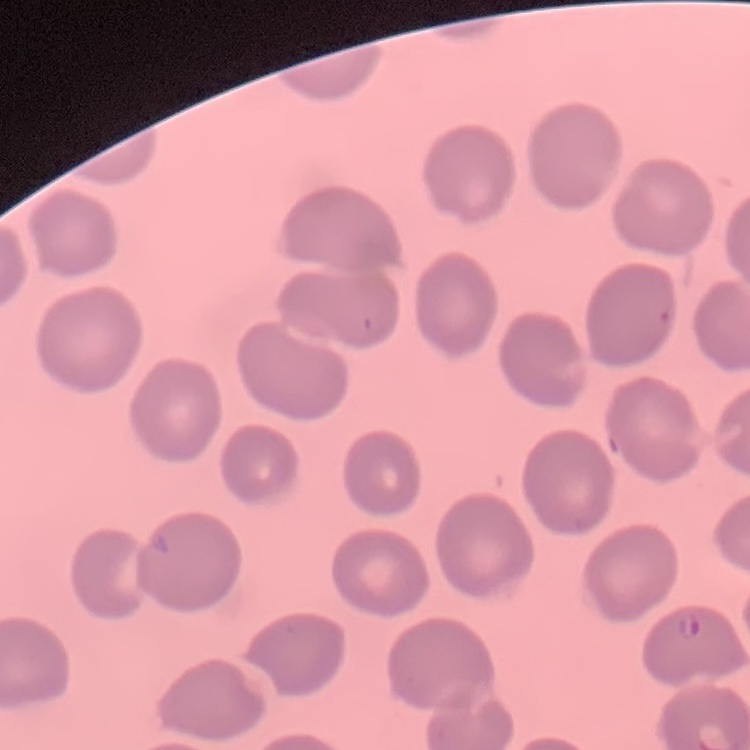
erythrocyte_morphology: no rouleaux formation
image_type: square crop of a larger photomicrograph
stain: Field's or Giemsa
preparation: thin blood film